Classify this cell by malaria status.
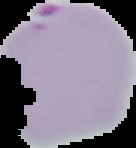

Parasitized.

Image is 136×148 pixels. The area outside the segmented cell region is set to black. From a thin blood smear.